Classify this cell by malaria status.
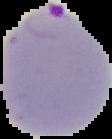

It is parasitized.

Summary:
  - Image type: segmented cell region with the area outside set to black
  - Preparation: thin blood smear
  - Image size: 112×139 pixels